State which parasite is depicted.
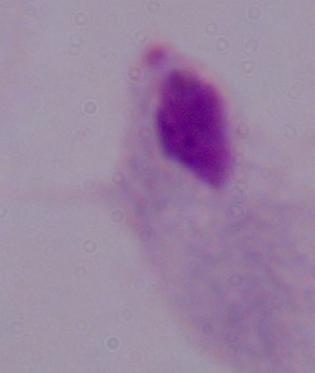
A trichomonad.

magnification = 1000x
modality = micrograph